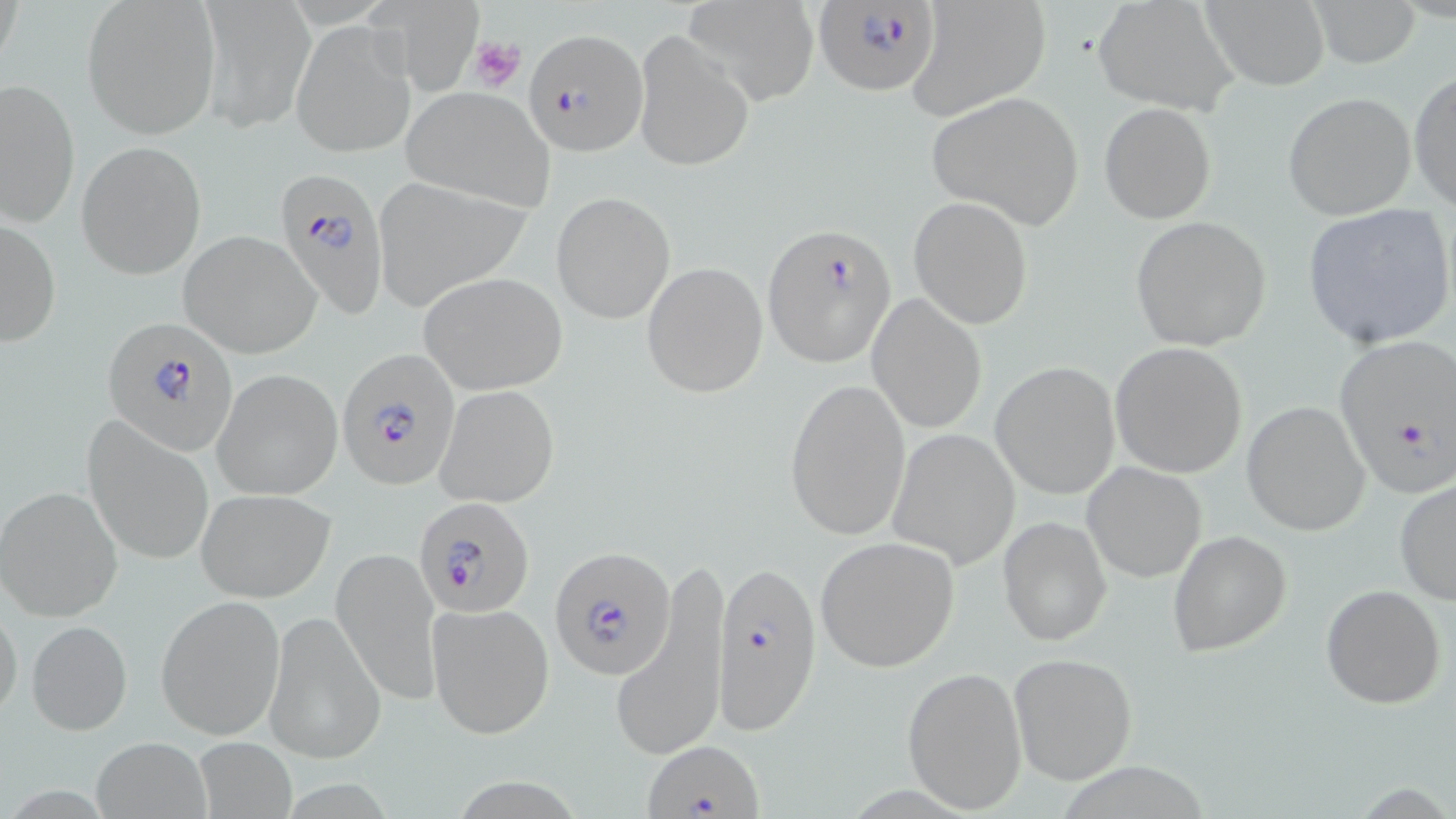

{
  "slide_level_diagnosis": "Plasmodium falciparum",
  "preparation": "thin blood smear",
  "uninfected_red_blood_cell_locations": "approximate bounding boxes as (x1,y1)-(x2,y2) corner pairs in pixels: (199,0)-(314,131), (685,0)-(819,103), (1093,0)-(1238,115), (1199,0)-(1330,90), (1304,0)-(1423,67), (81,1)-(221,138), (374,3)-(482,92), (908,3)-(1051,117), (292,19)-(415,158), (632,28)-(755,173), (1410,71)-(1456,208), (0,78)-(78,227), (401,86)-(556,211), (925,91)-(1085,229), (1283,92)-(1416,220), (1100,103)-(1216,223), (77,141)-(204,278), (371,179)-(532,313), (551,191)-(676,325), (908,196)-(1034,330), (1301,204)-(1455,350), (2,214)-(62,350), (1130,216)-(1272,350), (177,231)-(320,358), (640,261)-(768,399), (417,271)-(568,394), (868,293)-(987,435), (1109,341)-(1248,478), (990,361)-(1121,499), (213,369)-(345,499), (784,378)-(911,540), (435,383)-(560,508), (1242,401)-(1371,536), (85,421)-(213,565), (890,429)-(1020,570), (1083,462)-(1207,583), (1394,479)-(1456,604), (1,486)-(123,623), (195,489)-(336,602), (998,514)-(1112,647), (1169,530)-(1292,658), (814,536)-(960,672), (331,546)-(442,706), (614,565)-(730,767), (1320,585)-(1447,709), (155,595)-(285,739), (0,601)-(23,726), (427,601)-(554,738), (263,610)-(384,764), (26,619)-(132,736), (1009,651)-(1137,785), (902,665)-(1027,812), (91,736)-(213,819), (192,736)-(297,818)",
  "stain": "May-Grünwald-Giemsa",
  "platelet_locations": "approximate bounding boxes as (x1,y1)-(x2,y2) corner pairs in pixels: (469,36)-(526,93)",
  "modality": "light microscopy",
  "image_size": "1456×819 pixels",
  "magnification": "1000x",
  "plasmodium_falciparum_infected_red_blood_cell_locations": "approximate bounding boxes as (x1,y1)-(x2,y2) corner pairs in pixels: (813,1)-(943,96), (524,26)-(646,154), (277,167)-(391,319), (763,222)-(897,367), (106,321)-(238,451), (1331,333)-(1456,498), (337,348)-(463,490), (414,494)-(535,619), (550,547)-(673,679), (711,559)-(824,733), (645,741)-(764,817)",
  "field_of_view": "single"
}